Classify this cell by malaria status.
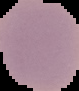

It is uninfected.

Image is 79×91 pixels. From a thin blood smear. Segmented cell region on a black background.